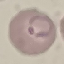 Result: malaria parasites identified. Giemsa stain. Photographed with a smartphone camera at the microscope eyepiece. Thin smear of blood. Cell patch, automatically extracted from a larger field of view and resized to 64 × 64 pixels.